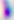
Summary:
  - Magnification: 400x
  - Identification: Toxoplasma gondii
  - Modality: photomicrograph